State which parasite is depicted.
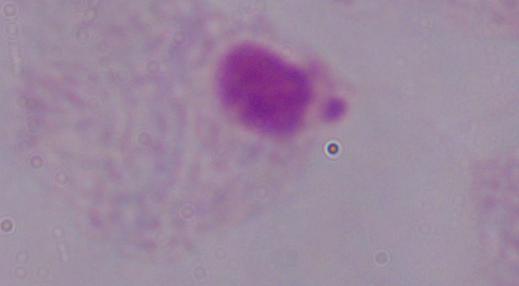
This is a trichomonad.

magnification = 1000x
modality = photomicrograph